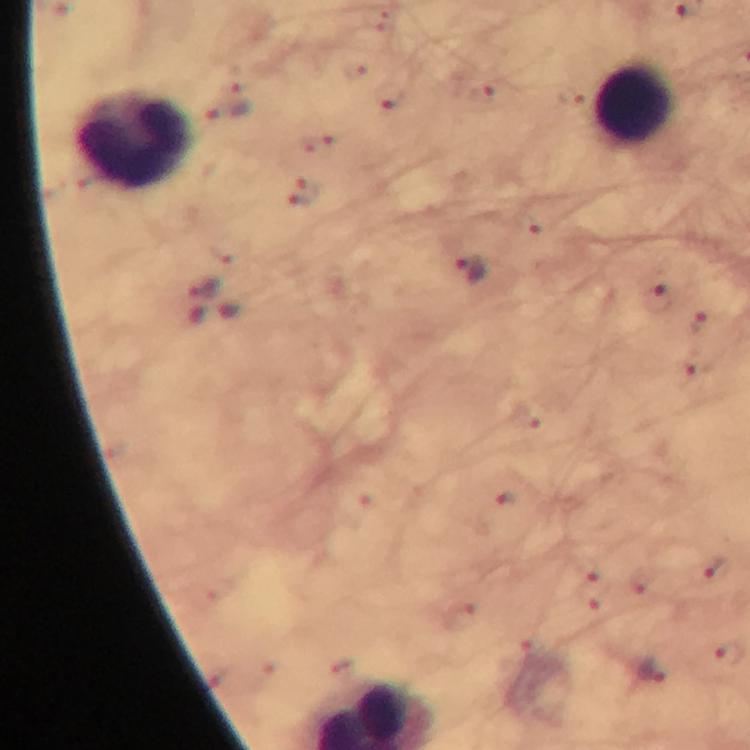 Approximate object centers, in pixels from the top-left corner. Plasmodium parasite locations: (x=483, y=92), (x=392, y=96), (x=227, y=110), (x=304, y=193), (x=470, y=270), (x=203, y=287), (x=659, y=298), (x=708, y=322), (x=695, y=366), (x=714, y=568), (x=728, y=652), (x=652, y=671). Leukocyte locations: (x=634, y=104), (x=133, y=140). Smartphone photograph taken through a microscope. Image is 750×750 pixels. Giemsa stain. At 100x magnification. A crop from one field of view. Immersion oil applied. Thick smear. From a diagnostic examination for malaria.